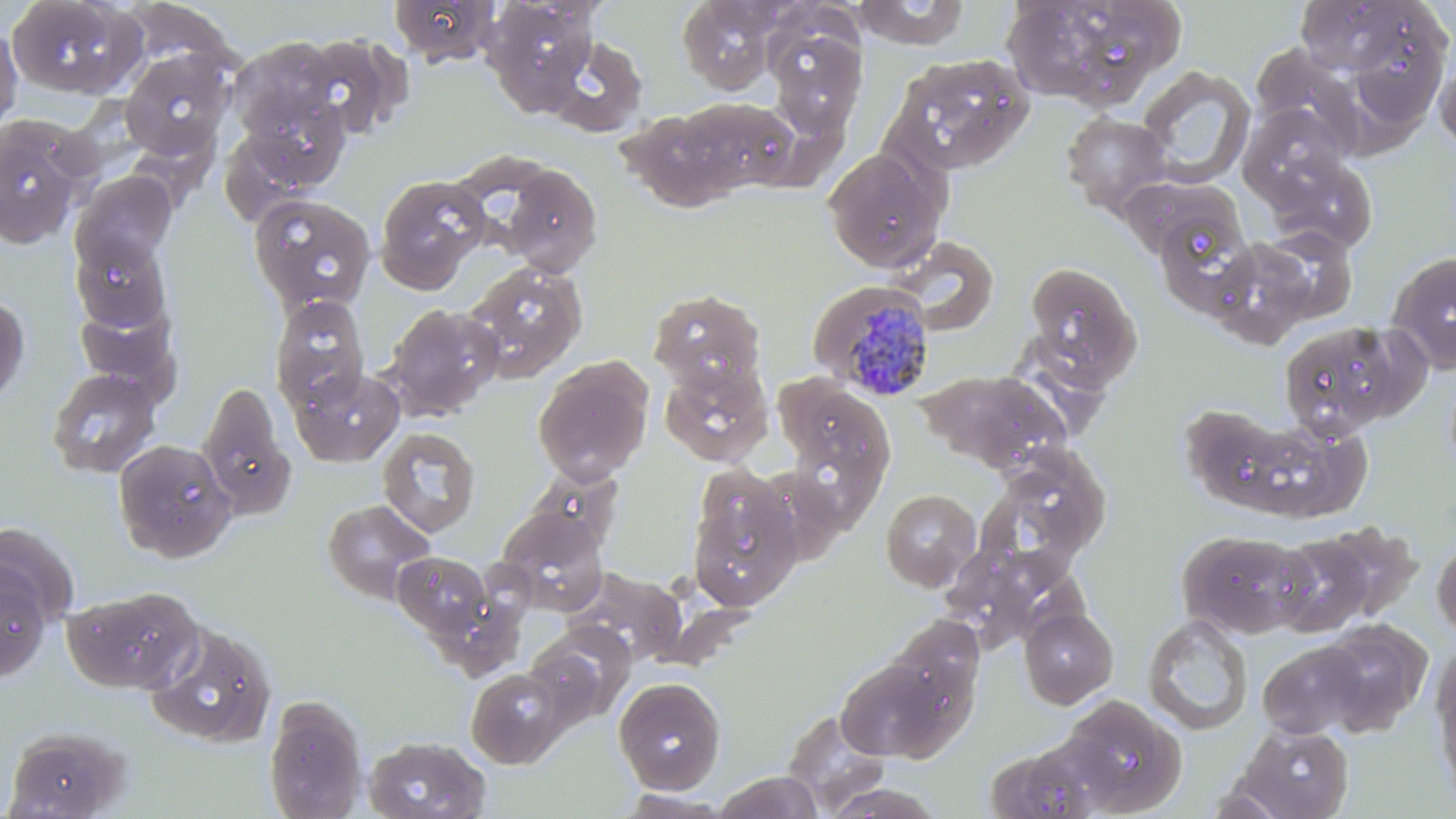

Approximate bounding boxes as (x1, y1, x2, y2) in pixels. Plasmodium malariae-infected red blood cell locations: (809, 280, 936, 401). Uninfected red blood cell locations: (4, 0, 142, 99), (389, 0, 500, 65), (678, 0, 779, 93), (852, 0, 970, 49), (1001, 0, 1103, 105), (1294, 0, 1416, 77), (484, 1, 598, 107), (1105, 2, 1190, 78), (1358, 6, 1448, 131), (1066, 17, 1156, 115), (0, 23, 23, 135), (778, 30, 867, 141), (294, 33, 408, 139), (545, 35, 648, 137), (227, 36, 344, 145), (1256, 44, 1373, 160), (119, 47, 234, 159), (887, 53, 1035, 175), (1435, 55, 1456, 153), (1133, 66, 1256, 189), (241, 92, 349, 191), (675, 97, 797, 193), (607, 100, 728, 212), (1248, 103, 1350, 203), (1060, 111, 1176, 219), (0, 115, 85, 248), (822, 147, 947, 272), (1276, 159, 1381, 245), (500, 163, 603, 275), (1114, 168, 1248, 262), (71, 171, 176, 273), (374, 175, 489, 293), (249, 194, 377, 315), (1158, 214, 1253, 322), (889, 236, 1000, 336), (71, 238, 171, 331), (1215, 239, 1323, 348), (1385, 250, 1456, 375), (464, 260, 588, 382), (1022, 260, 1144, 385), (648, 288, 766, 392), (0, 292, 30, 408), (269, 295, 371, 414), (384, 302, 502, 420), (1277, 320, 1422, 440), (1001, 330, 1125, 436), (533, 356, 654, 485), (659, 361, 773, 467), (46, 367, 161, 478), (291, 367, 404, 466), (916, 369, 1071, 474), (777, 377, 895, 487), (197, 380, 294, 519), (1186, 396, 1310, 515), (1255, 415, 1372, 523), (377, 427, 480, 538), (112, 439, 237, 562), (517, 468, 624, 561), (987, 470, 1093, 592), (687, 473, 803, 613), (880, 488, 982, 592), (321, 499, 437, 606), (497, 508, 608, 614), (1315, 521, 1422, 622), (0, 524, 78, 630), (1177, 529, 1314, 638), (1272, 532, 1378, 637), (1432, 533, 1456, 640), (393, 551, 493, 640), (0, 563, 52, 682), (556, 566, 690, 670), (63, 586, 203, 694), (1019, 607, 1118, 708), (881, 613, 986, 729), (1143, 614, 1253, 735), (1318, 619, 1432, 734), (143, 620, 277, 748), (525, 638, 613, 725), (1257, 640, 1370, 739), (1430, 647, 1456, 802), (834, 655, 961, 763), (466, 668, 565, 768), (613, 676, 727, 794), (264, 695, 369, 818), (1061, 695, 1188, 815), (781, 708, 893, 816), (1233, 721, 1354, 818), (4, 725, 130, 818), (363, 735, 492, 819), (985, 735, 1120, 819), (713, 771, 824, 819), (819, 783, 947, 818), (1198, 783, 1295, 818), (614, 790, 736, 818). Slide-level diagnosis: Plasmodium malariae. Image is 1456×819 pixels. 1000x magnification. Single field of view. May-Grünwald-Giemsa stain. Thin blood film. Light microscopy.